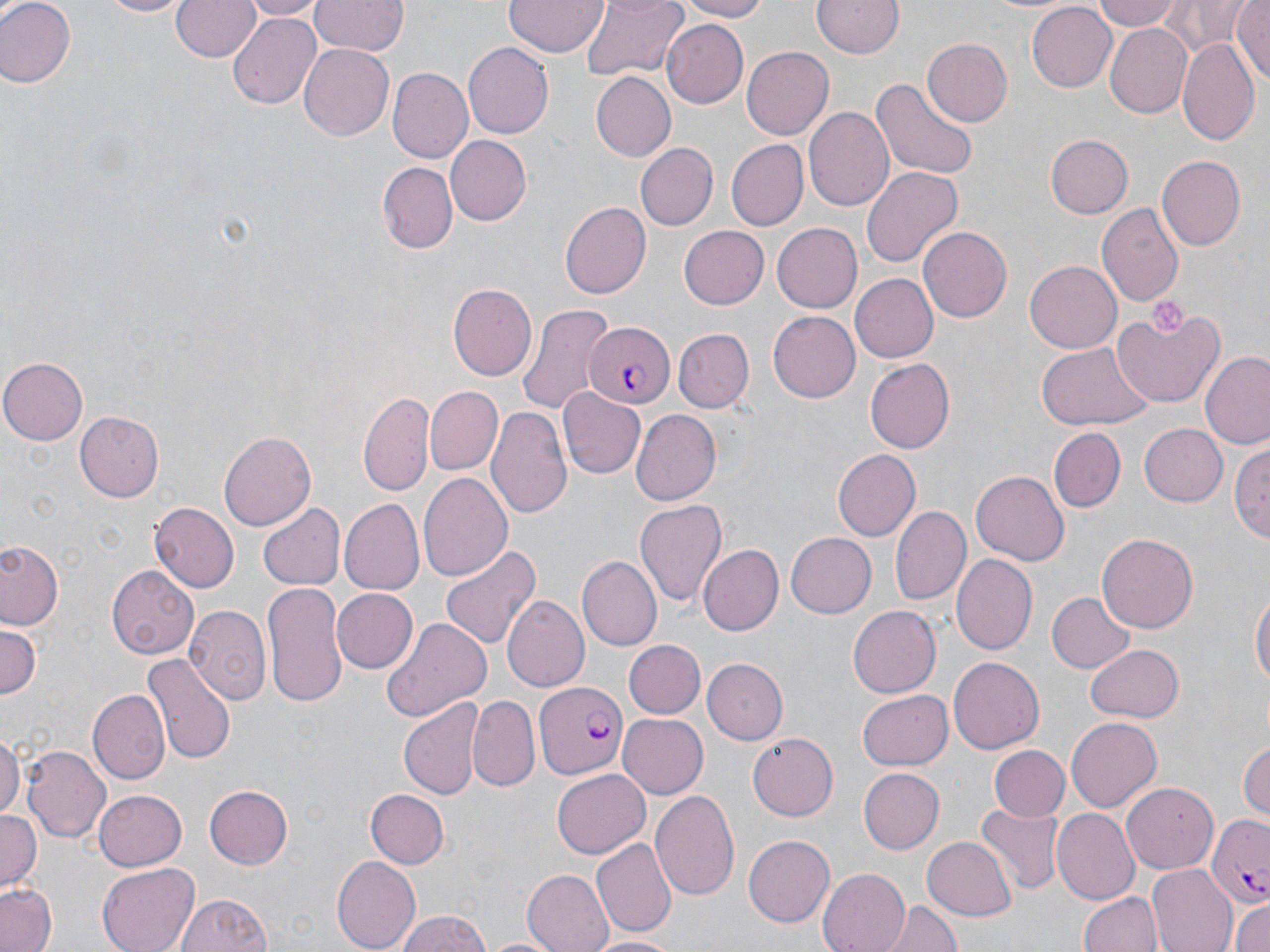

Approximate bounding boxes as (x1, y1, x2, y2) in pixels. Platelet locations: (1147, 299, 1187, 334). Uninfected red blood cell locations: (0, 0, 75, 88), (99, 0, 192, 18), (170, 0, 259, 64), (238, 0, 323, 18), (310, 0, 407, 57), (505, 0, 607, 58), (578, 0, 687, 82), (671, 0, 775, 21), (1092, 0, 1180, 30), (1230, 0, 1268, 86), (811, 1, 903, 58), (1026, 2, 1115, 89), (1164, 3, 1259, 54), (229, 12, 322, 111), (660, 18, 748, 107), (1104, 22, 1195, 119), (1178, 37, 1259, 148), (923, 39, 1012, 125), (297, 43, 394, 141), (462, 43, 552, 138), (740, 45, 833, 137), (389, 68, 474, 164), (589, 72, 676, 163), (870, 78, 978, 180), (803, 104, 893, 209), (1044, 134, 1131, 218), (444, 136, 530, 226), (724, 140, 808, 230), (633, 143, 717, 231), (1156, 156, 1245, 252), (378, 162, 455, 254), (862, 166, 963, 271), (560, 200, 651, 297), (1096, 203, 1183, 306), (771, 221, 862, 311), (678, 223, 769, 307), (918, 225, 1011, 323), (1025, 260, 1122, 352), (850, 274, 938, 362), (448, 283, 536, 379), (518, 302, 616, 418), (1112, 305, 1224, 409), (768, 311, 861, 403), (672, 328, 752, 413), (1036, 341, 1151, 431), (1200, 351, 1270, 451), (1, 358, 88, 443), (865, 358, 955, 454), (559, 387, 647, 479), (359, 389, 435, 497), (425, 389, 503, 476), (488, 405, 574, 520), (629, 410, 721, 505), (74, 412, 164, 501), (1138, 422, 1227, 506), (1048, 428, 1126, 513), (219, 432, 315, 529), (1230, 438, 1270, 543), (833, 449, 922, 541), (972, 470, 1069, 567), (418, 472, 513, 582), (341, 499, 427, 594), (635, 500, 727, 608), (889, 501, 970, 605), (150, 502, 240, 591), (258, 503, 344, 590), (786, 532, 878, 618), (1098, 533, 1198, 635), (437, 540, 540, 653), (0, 541, 65, 631), (696, 544, 782, 635), (953, 555, 1037, 654), (577, 556, 661, 650), (105, 565, 199, 661), (263, 583, 347, 706), (329, 587, 417, 675), (1251, 588, 1269, 696), (1046, 592, 1134, 673), (501, 597, 590, 692), (848, 604, 940, 696), (185, 606, 273, 703), (382, 616, 493, 719), (0, 625, 41, 704), (623, 639, 705, 719), (1085, 641, 1184, 720), (142, 653, 236, 762), (947, 656, 1043, 754), (703, 657, 788, 743), (858, 690, 953, 771), (90, 691, 167, 782), (469, 697, 539, 790), (399, 699, 483, 800), (616, 714, 706, 798), (1065, 717, 1162, 811), (0, 729, 21, 821), (747, 732, 839, 820), (1237, 738, 1270, 821), (24, 747, 110, 843), (988, 747, 1068, 820), (857, 768, 942, 853), (550, 770, 650, 858), (1122, 781, 1219, 872), (204, 784, 294, 868), (364, 788, 449, 868), (651, 790, 739, 899), (93, 791, 186, 870), (976, 803, 1063, 894), (1051, 808, 1140, 903), (0, 809, 40, 894), (921, 832, 1017, 921), (743, 835, 834, 926), (591, 839, 675, 937), (330, 854, 419, 952), (96, 862, 200, 952), (1146, 864, 1236, 952), (816, 868, 911, 952), (521, 870, 612, 952), (0, 883, 58, 952), (175, 888, 278, 952), (1077, 890, 1162, 952), (879, 898, 964, 950), (1229, 899, 1270, 952), (392, 909, 495, 952), (585, 933, 685, 951). Plasmodium falciparum-infected red blood cell locations: (582, 320, 673, 406), (536, 680, 628, 781), (1206, 815, 1268, 909). Slide-level diagnosis: Plasmodium falciparum. Light microscopy. Thin blood film. May-Grünwald-Giemsa stain. Image is 1270×952 pixels. Single field of view. Captured at 1000x magnification.